Classify this cell by malaria status.
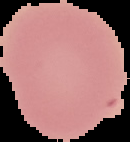

Uninfected.

Image is 130×142 pixels. From a thin blood film. Segmented cell region on a black background.